Outline each blood parasite and name the species.
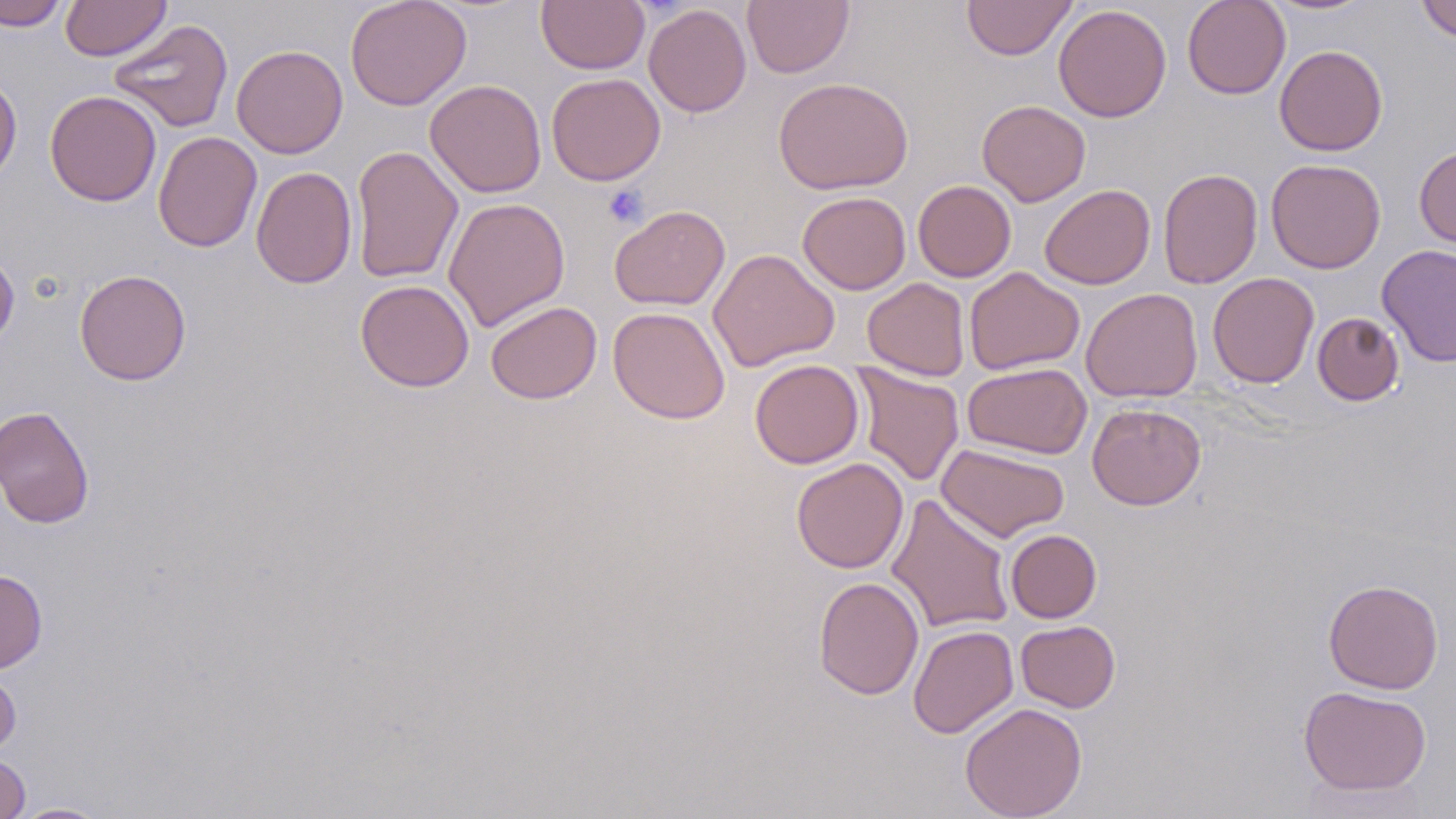

No blood parasites observed.

Approximate bounding boxes as (x1, y1, x2, y2) in pixels. Uninfected red blood cell locations: (0, 0, 69, 30), (60, 0, 170, 61), (345, 0, 472, 111), (537, 0, 649, 74), (961, 0, 1077, 61), (1182, 0, 1291, 100), (1259, 0, 1380, 16), (1416, 0, 1456, 42), (742, 1, 853, 78), (643, 4, 752, 117), (1053, 4, 1171, 122), (107, 19, 234, 133), (231, 44, 348, 158), (1274, 44, 1388, 156), (546, 72, 666, 185), (0, 75, 22, 186), (773, 76, 913, 195), (425, 79, 546, 198), (45, 90, 162, 206), (977, 99, 1091, 206), (153, 131, 262, 253), (350, 145, 464, 285), (1415, 145, 1456, 249), (1265, 158, 1386, 273), (251, 166, 357, 289), (1157, 168, 1263, 289), (913, 180, 1016, 282), (1040, 184, 1155, 289), (797, 191, 911, 294), (443, 197, 570, 332), (609, 205, 730, 311), (1377, 243, 1456, 367), (708, 248, 839, 371), (0, 249, 19, 351), (963, 267, 1085, 375), (74, 268, 191, 385), (1208, 272, 1319, 388), (862, 277, 970, 381), (355, 279, 474, 392), (1081, 287, 1203, 403), (485, 301, 602, 404), (608, 306, 730, 424), (1312, 312, 1404, 406), (750, 359, 864, 469), (963, 362, 1092, 459), (851, 363, 964, 486), (1087, 403, 1206, 510), (0, 405, 95, 527), (936, 442, 1070, 542), (792, 458, 908, 573), (886, 494, 1015, 634), (1005, 529, 1101, 622), (0, 569, 47, 673), (813, 576, 924, 700), (1322, 578, 1444, 694), (1015, 620, 1120, 712), (908, 624, 1019, 738), (0, 669, 21, 758), (1298, 685, 1432, 796), (960, 702, 1087, 819), (0, 755, 30, 819), (12, 802, 110, 818). Platelet locations: (604, 185, 649, 229). Slide-level diagnosis: no evidence of blood parasites. Image is 1456×819 pixels. Single field of view. Thin blood smear. Optical microscopy. 1000x magnification. May-Grünwald-Giemsa-stained preparation.